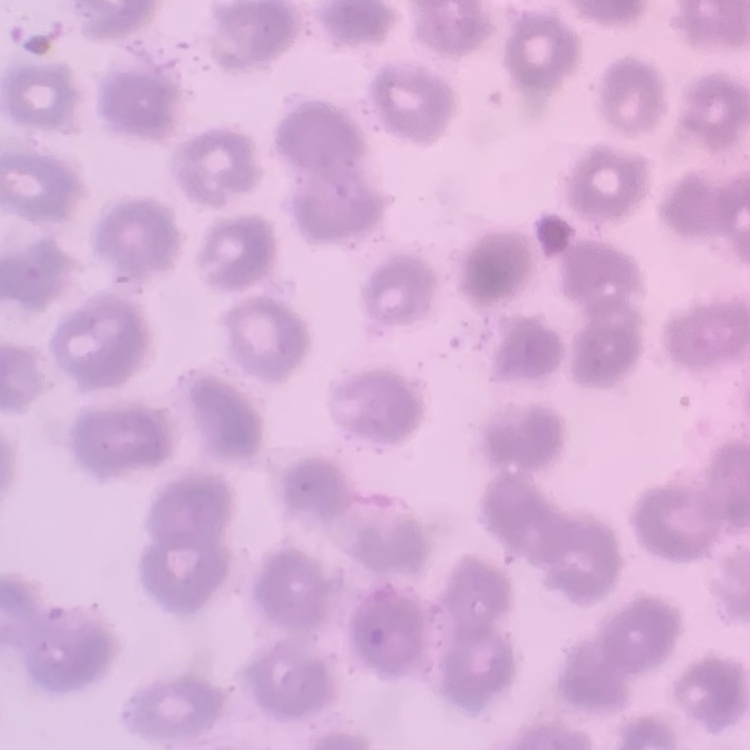

{
  "erythrocyte_morphology": "no rouleaux formation",
  "image_type": "square crop of a larger photomicrograph",
  "stain": "Field's or Giemsa",
  "preparation": "thin blood smear"
}